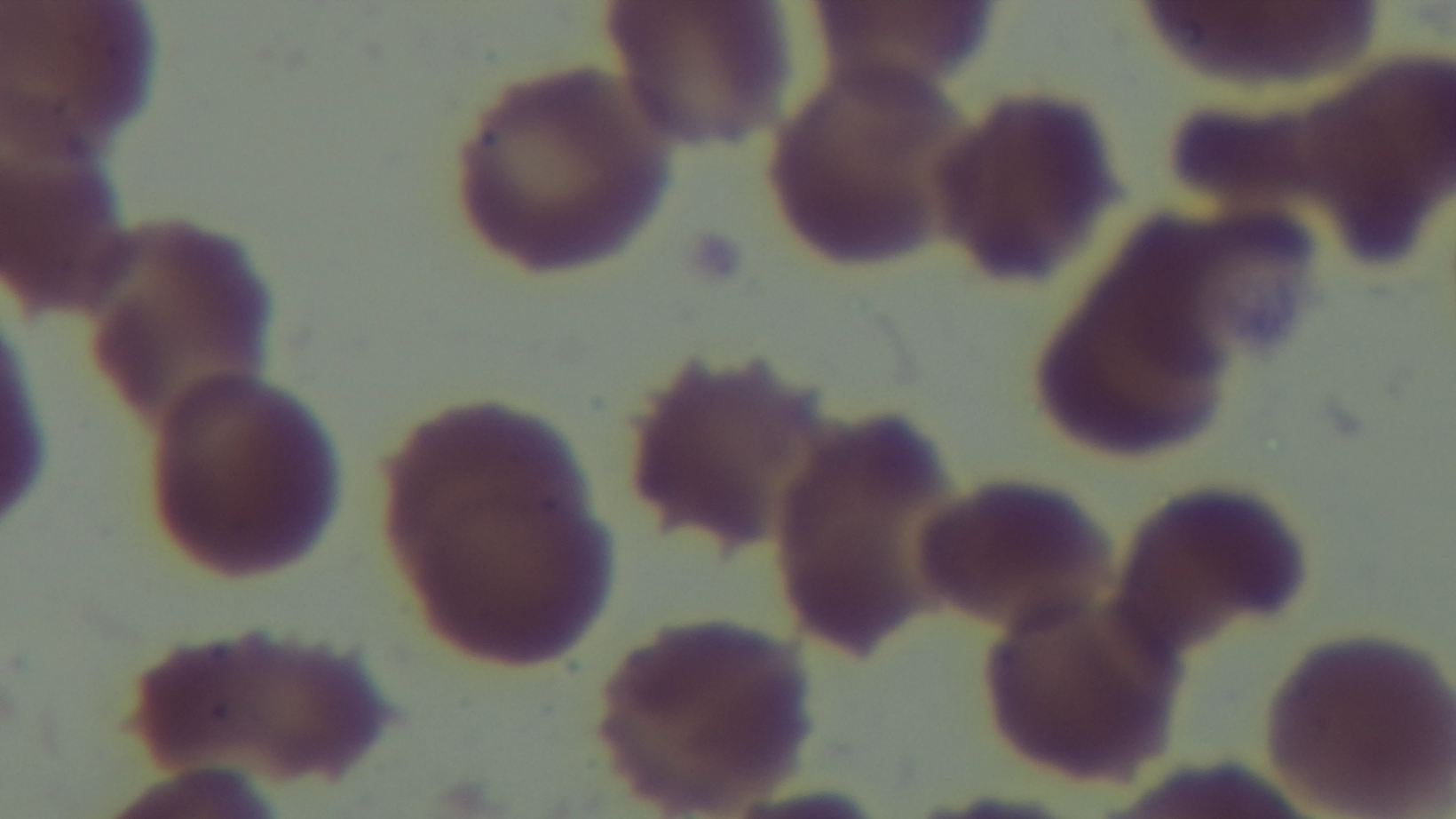

Summary:
  - Modality: light microscopy
  - Field of view: single
  - Preparation: thin
  - Capture: mounted 4K digital camera
  - Stain: Giemsa
  - Malaria status: negative
  - Objective: 100x oil immersion